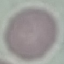

Summary:
  - Result: negative for malaria parasites
  - Preparation: thin smear
  - Capture: smartphone camera at the microscope eyepiece
  - Image type: automatically extracted cell patch, resized to 64 × 64 pixels
  - Stain: Giemsa